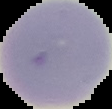

From a thin blood smear. Cell region segmented out of the field of view; the surrounding area is masked to black. Image is 112×109 pixels. Result: no Plasmodium parasites seen.